Identify the parasite.
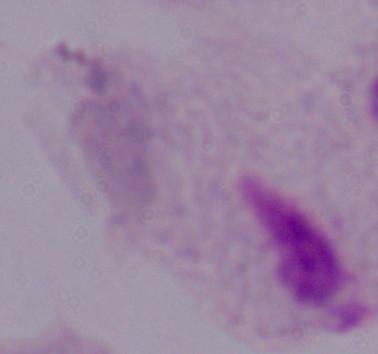

A trichomonad.

1000x magnification. Micrograph.